Assess this cell for malaria.
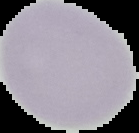
Uninfected.

From a thin blood smear. Image is 139×133 pixels. Cell region segmented out of the field of view; the surrounding area is masked to black.